Point out each leukocyte.
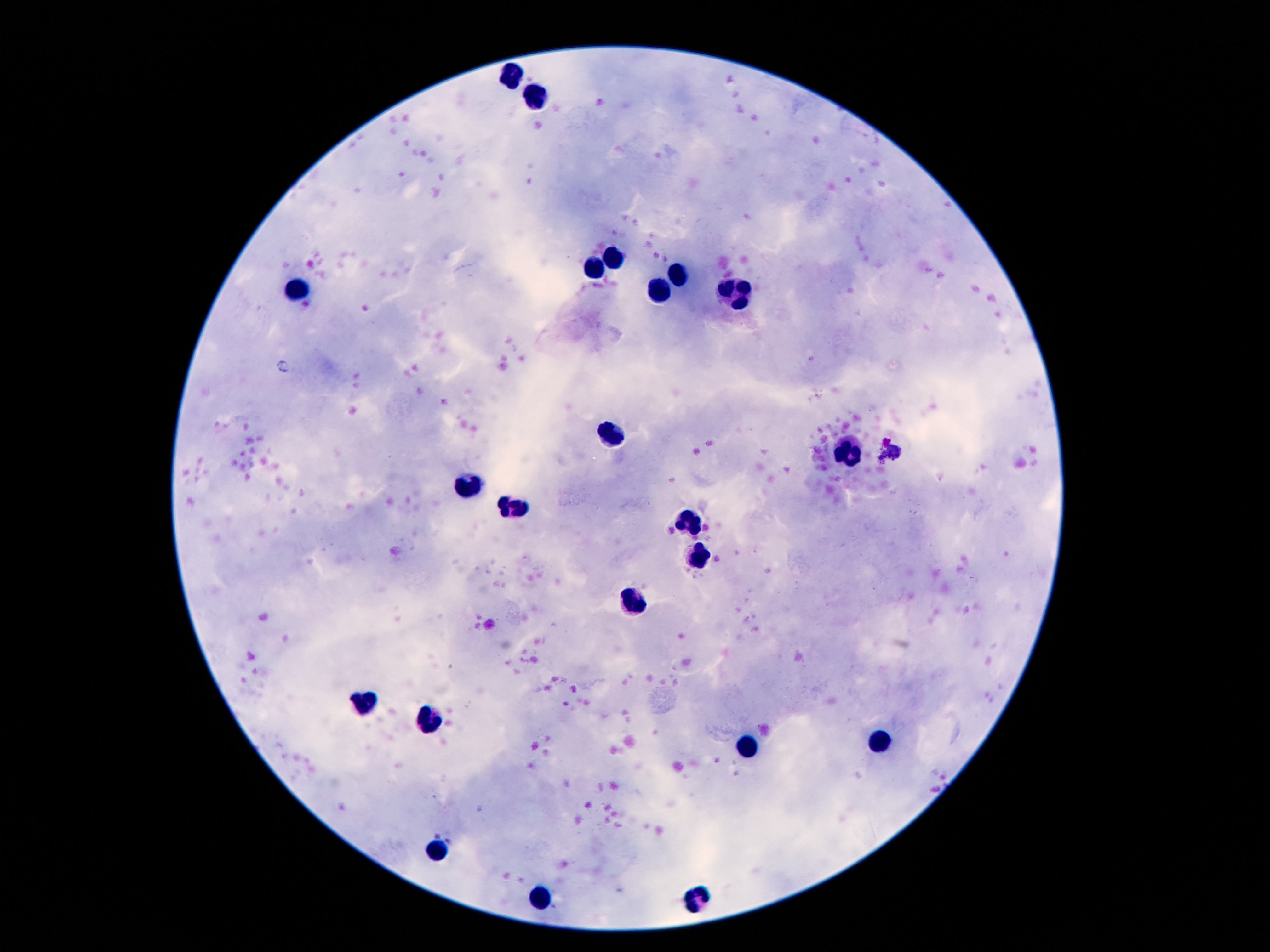

Approximate centers as [x, y] in pixels.
Leukocytes: [511, 77], [534, 95], [613, 260], [595, 270], [678, 274], [296, 291], [662, 295], [739, 295], [609, 434], [847, 452], [469, 485], [515, 508], [689, 519], [699, 555], [634, 600], [365, 706], [433, 719], [881, 741], [750, 748], [435, 849], [541, 898], [697, 898].

Summary:
  - Capture: smartphone camera through the microscope eyepiece
  - Image size: 1270×952 pixels
  - Magnification: 100x
  - Preparation: thick peripheral-blood smear
  - Field of view: single
  - Patient malaria status: negative
  - Stain: Giemsa